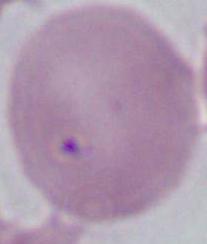

Photomicrograph. 1000x magnification. A red blood cell is seen.